Evaluate for malaria.
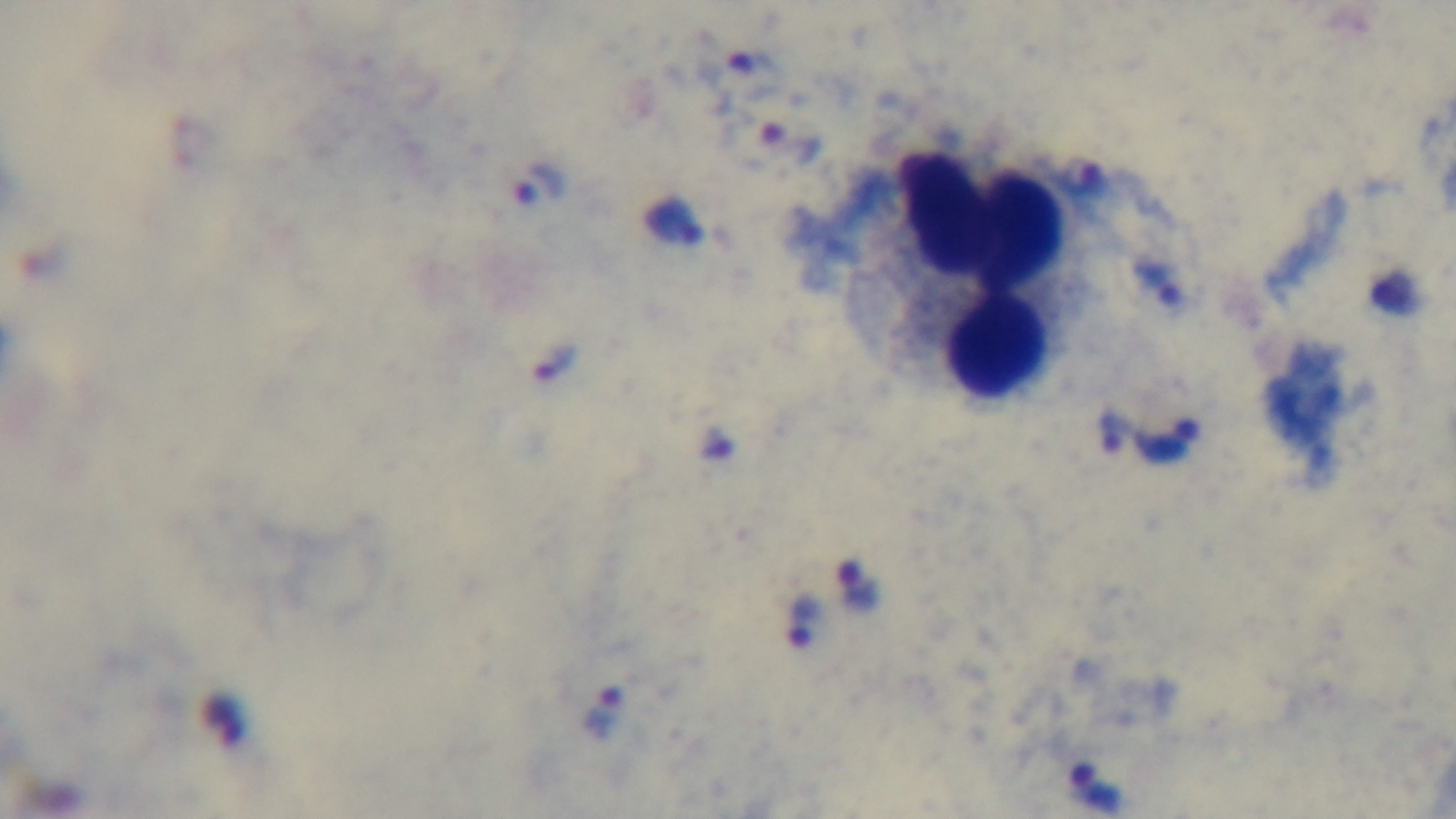
Infected.

Preparation: thick blood film. 100x oil-immersion objective. Photomicrograph. Single field of view. Giemsa-stained. Captured with a mounted 4K digital camera.